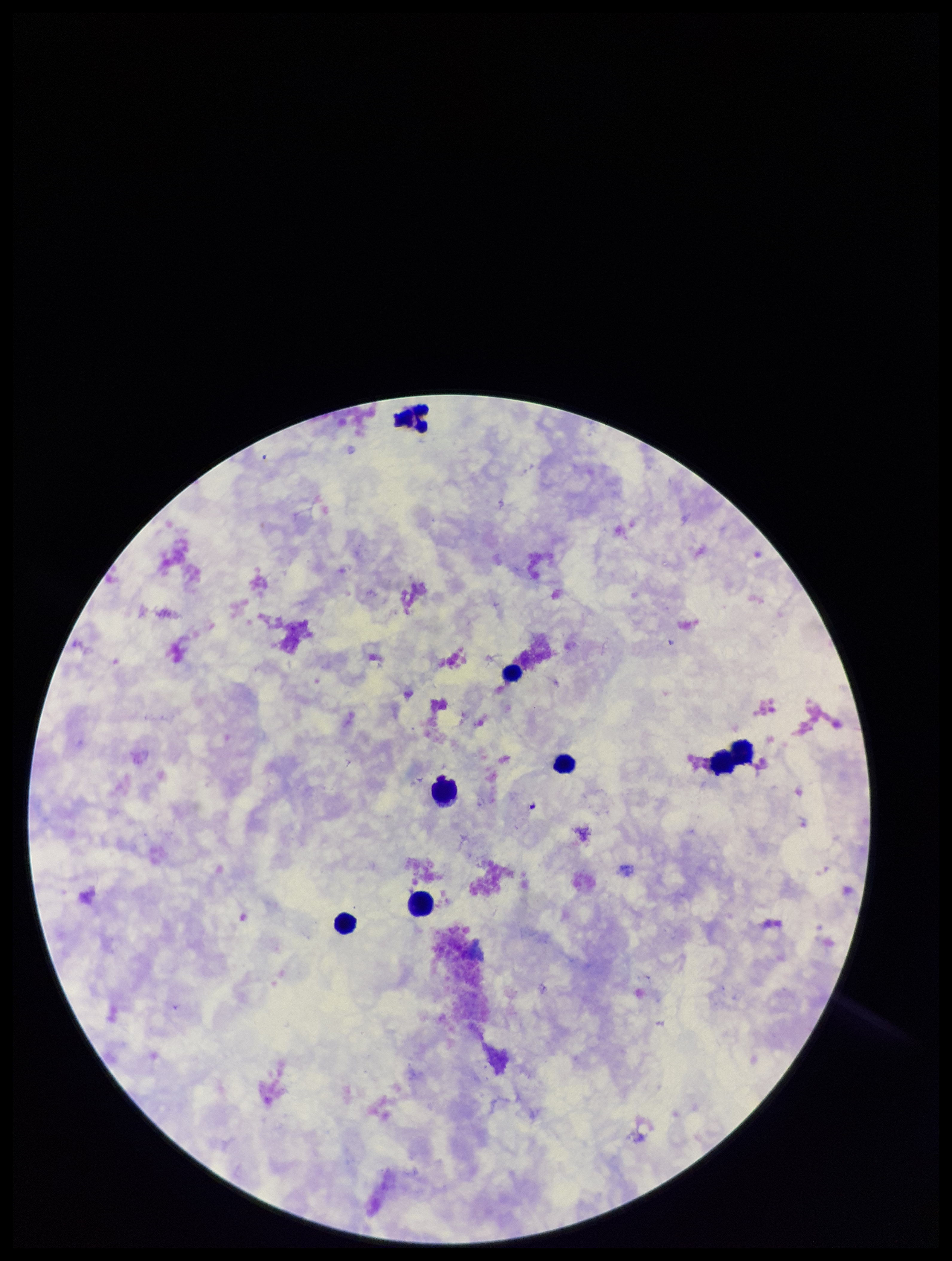

Preparation: thick smear. Leukocyte count: 7. Stained with Giemsa. Parasite count: 0. Image is 952×1261 pixels. Smartphone photograph taken through the eyepiece of a microscope. Plasmodium parasites: none identified. One field from this slide. Patient malaria status: negative.